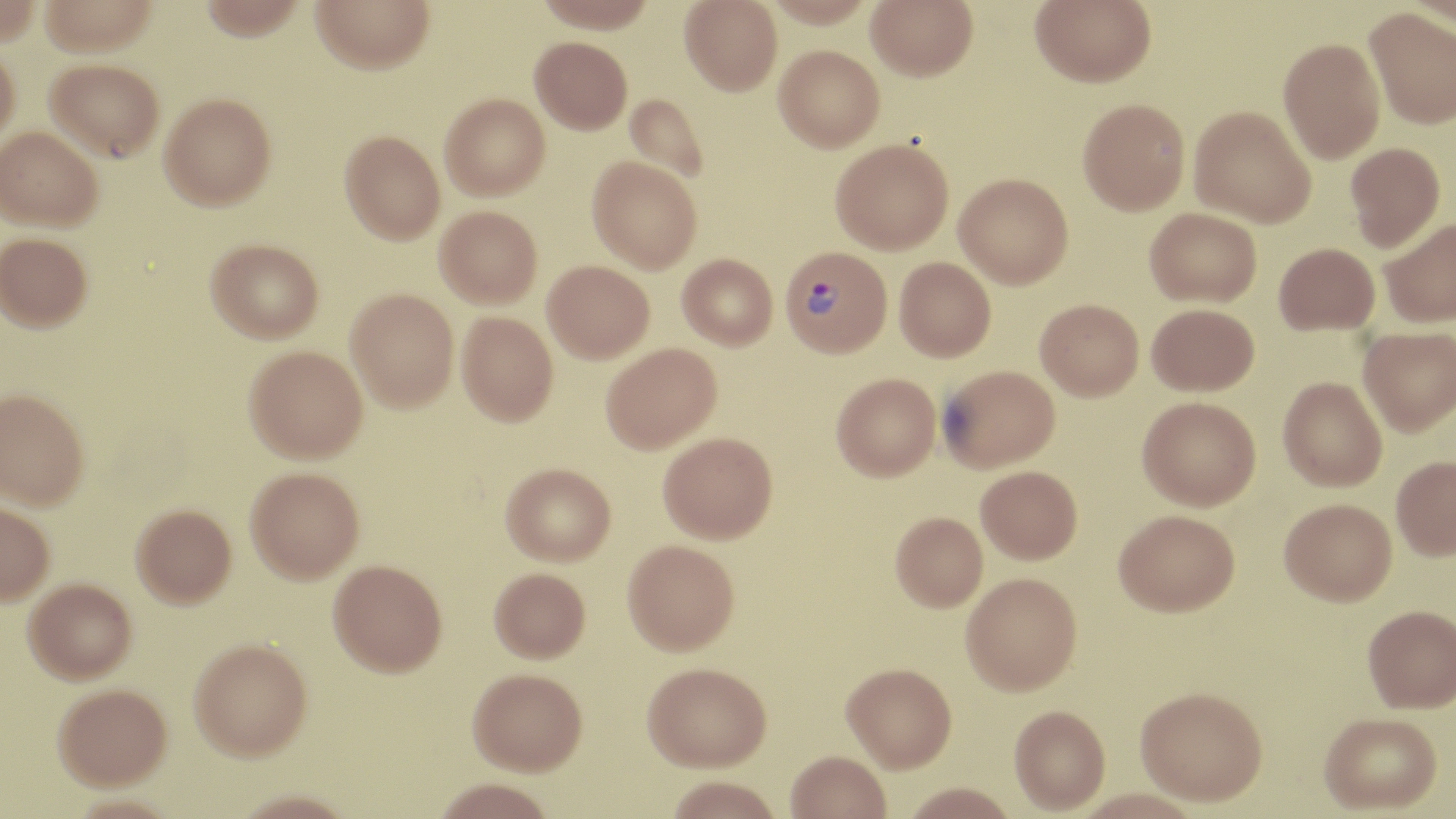
Summary:
  - Coordinate format: approximate bounding boxes as [x1, y1, x2, y2] in pixels
  - Uninfected red blood cell locations: [38, 0, 160, 56], [197, 0, 308, 39], [311, 0, 434, 73], [535, 0, 657, 33], [680, 0, 782, 95], [763, 0, 874, 28], [866, 0, 978, 80], [1030, 0, 1156, 87], [1403, 0, 1456, 31], [1365, 7, 1456, 129], [530, 36, 632, 134], [1278, 37, 1385, 164], [0, 42, 20, 143], [773, 45, 884, 152], [45, 58, 164, 161], [160, 92, 276, 209], [441, 93, 550, 200], [624, 93, 710, 184], [1078, 98, 1190, 215], [1188, 105, 1316, 228], [1, 127, 103, 231], [340, 131, 445, 244], [830, 139, 953, 254], [1344, 142, 1445, 251], [587, 156, 702, 273], [954, 173, 1073, 288], [435, 205, 542, 308], [1145, 207, 1261, 307], [1379, 216, 1456, 328], [0, 232, 93, 331], [206, 238, 324, 342], [1274, 243, 1379, 335], [677, 253, 777, 350], [894, 257, 996, 361], [542, 260, 654, 363], [346, 288, 458, 412], [1035, 299, 1143, 400], [1146, 303, 1259, 396], [456, 311, 558, 425], [1358, 325, 1456, 436], [601, 342, 722, 454], [244, 345, 367, 462], [938, 364, 1060, 471], [831, 372, 940, 481], [1278, 377, 1387, 491], [1, 387, 90, 509], [1137, 396, 1261, 511], [658, 432, 778, 543], [1391, 455, 1456, 560], [501, 462, 616, 565], [976, 465, 1082, 564], [245, 466, 364, 583], [1279, 498, 1397, 606], [0, 499, 55, 605], [131, 503, 236, 607], [1114, 509, 1240, 617], [890, 512, 988, 613], [623, 539, 740, 655], [328, 559, 447, 676], [489, 566, 590, 662], [962, 575, 1082, 698], [24, 577, 137, 683], [1362, 605, 1456, 714], [189, 637, 312, 759], [642, 663, 772, 774], [841, 665, 957, 776], [466, 668, 587, 775], [53, 682, 172, 789], [1134, 692, 1267, 812], [1009, 709, 1110, 816], [1319, 715, 1443, 817], [785, 752, 891, 819], [664, 778, 783, 819], [431, 779, 558, 819], [901, 785, 1019, 819], [1072, 791, 1205, 818]
  - Plasmodium vivax-infected red blood cell locations: [779, 246, 893, 358]
  - Slide-level diagnosis: Plasmodium vivax
  - Modality: optical microscopy
  - Stain: May-Grünwald-Giemsa
  - Field of view: one of a larger specimen
  - Preparation: thin blood smear
  - Image size: 1456×819 pixels
  - Magnification: 1000x